Identify the parasite.
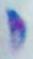

Toxoplasma gondii.

{
  "modality": "micrograph",
  "magnification": "1000x"
}